Identify the preparation type.
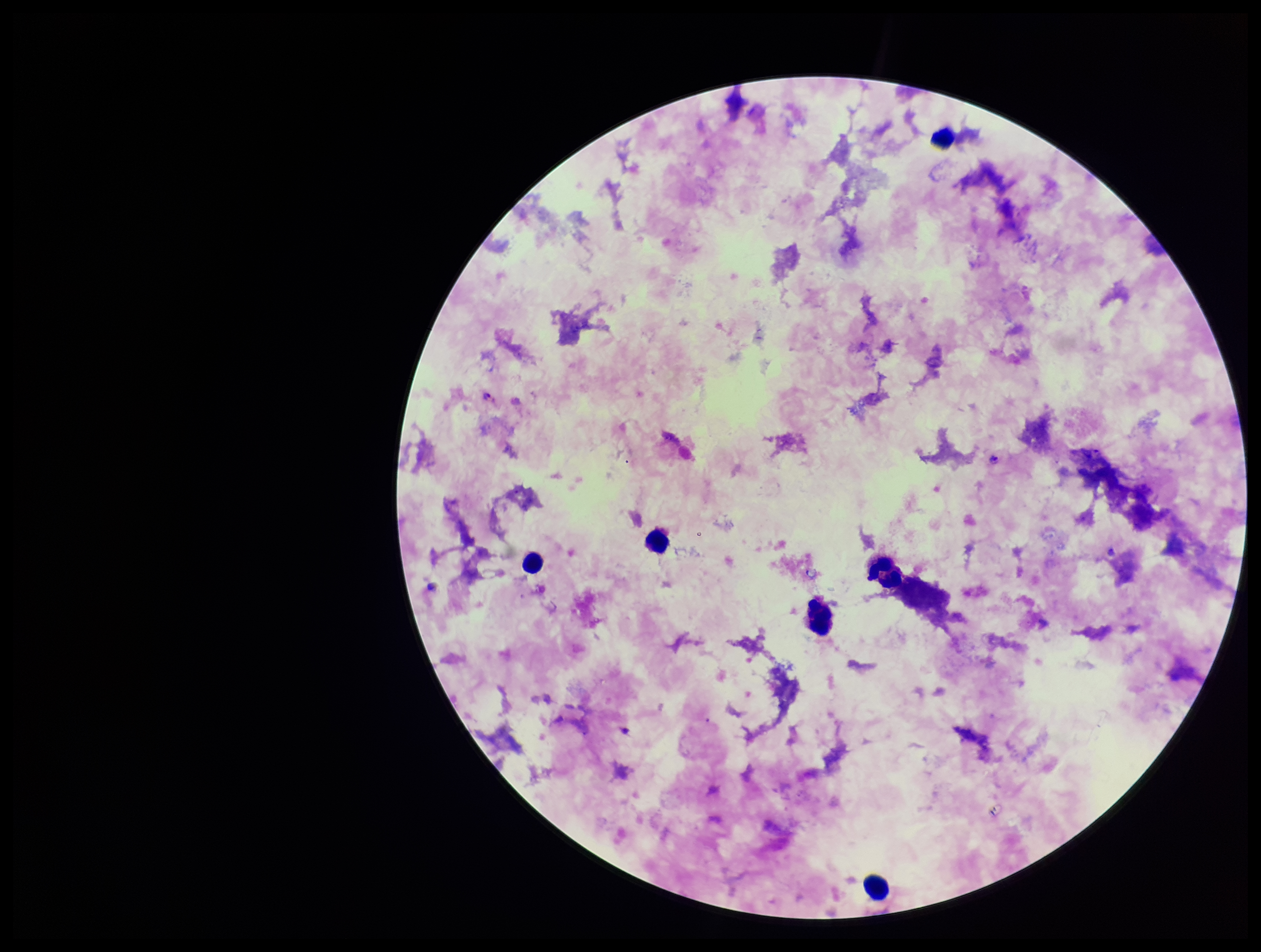
It is a thick blood smear.

Summary:
  - Image size: 1261×952 pixels
  - Field of view: one from this slide
  - Species reported for this patient: Plasmodium falciparum
  - Parasite count: 2
  - Stain: Giemsa
  - Capture: smartphone photograph through the microscope eyepiece
  - Plasmodium parasites: seen
  - Patient malaria status: positive
  - Leukocyte count: 5